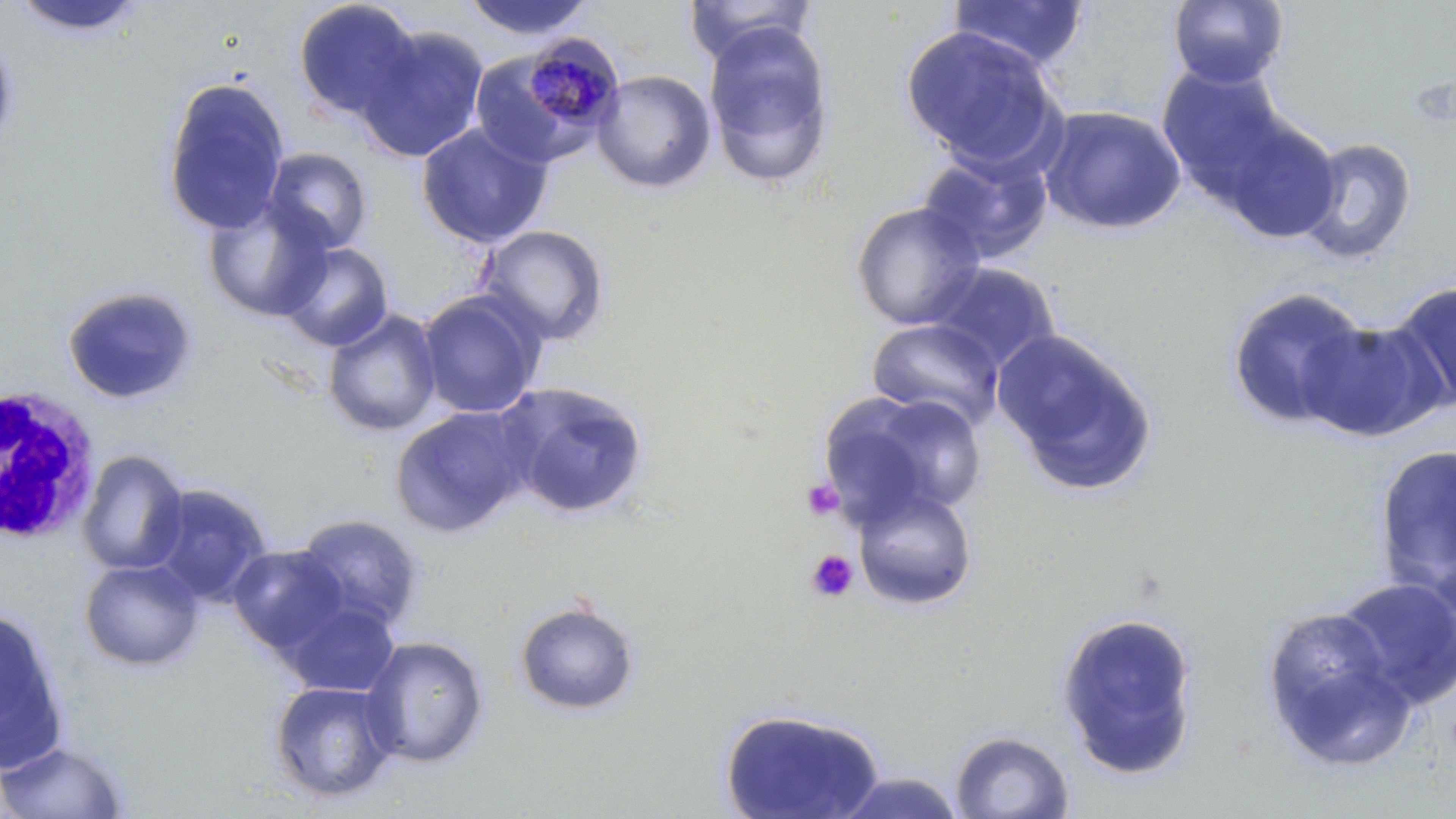
{
  "slide_level_diagnosis": "Plasmodium malariae",
  "white_blood_cell_locations": "approximate bounding boxes as (x1,y1)-(x2,y2) corner pairs in pixels: (2,385)-(103,547)",
  "plasmodium_malariae_infected_red_blood_cell_locations": "approximate bounding boxes as (x1,y1)-(x2,y2) corner pairs in pixels: (519,35)-(625,136)",
  "magnification": "1000x",
  "field_of_view": "one of a larger specimen",
  "platelet_locations": "approximate bounding boxes as (x1,y1)-(x2,y2) corner pairs in pixels: (802,478)-(844,522), (806,549)-(858,602)",
  "modality": "optical microscopy",
  "preparation": "thin blood smear",
  "uninfected_red_blood_cell_locations": "approximate bounding boxes as (x1,y1)-(x2,y2) corner pairs in pixels: (7,0)-(151,39), (292,0)-(421,121), (461,0)-(596,41), (683,0)-(818,65), (1166,0)-(1289,89), (946,1)-(1090,71), (703,23)-(836,189), (355,25)-(490,163), (901,26)-(1062,169), (0,27)-(18,158), (1157,63)-(1291,199), (592,69)-(716,193), (161,76)-(290,235), (1038,105)-(1188,236), (1219,117)-(1341,244), (416,121)-(553,249), (1295,136)-(1417,265), (262,147)-(373,254), (917,148)-(1054,265), (202,196)-(335,323), (850,201)-(987,330), (476,224)-(610,346), (277,242)-(393,352), (928,263)-(1061,375), (1387,278)-(1456,415), (61,285)-(199,406), (1225,286)-(1375,431), (417,290)-(546,419), (323,308)-(442,437), (866,318)-(1006,432), (1301,318)-(1446,443), (992,329)-(1158,496), (496,381)-(650,520), (824,390)-(987,522), (390,404)-(536,538), (1373,442)-(1456,604), (77,449)-(189,576), (144,482)-(272,607), (851,483)-(978,611), (293,513)-(426,633), (227,545)-(349,656), (79,559)-(206,671), (1331,576)-(1456,711), (278,596)-(402,698), (513,598)-(641,717), (0,606)-(69,773), (1260,607)-(1416,772), (1055,610)-(1200,779), (360,635)-(489,768), (268,679)-(402,804), (719,706)-(887,819), (949,729)-(1074,818), (0,740)-(132,818), (832,771)-(967,817)",
  "image_size": "1456×819 pixels",
  "stain": "May-Grünwald-Giemsa"
}